Point out each Plasmodium parasite.
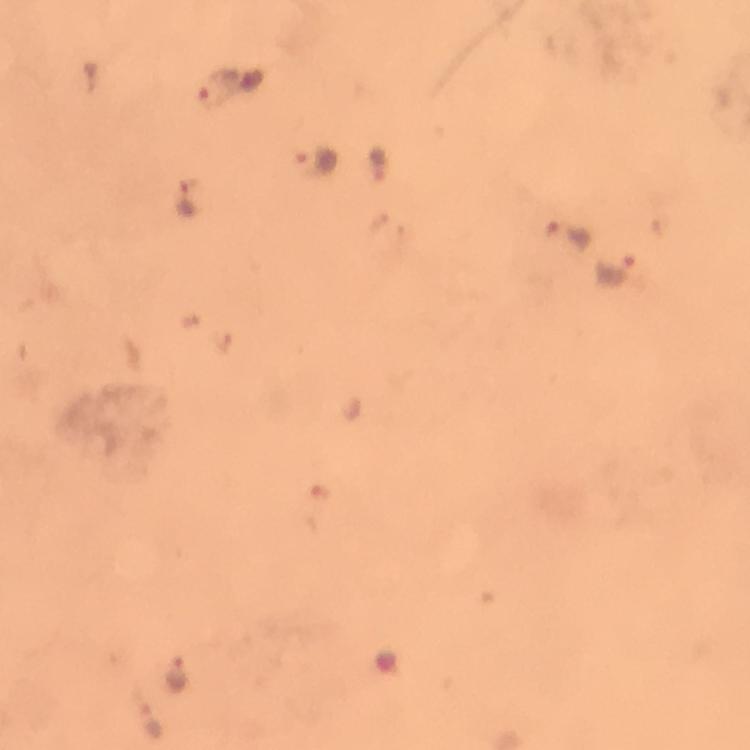

Approximate object centers, in pixels from the top-left corner.
Plasmodium parasites: (x=231, y=91), (x=318, y=163), (x=189, y=199), (x=568, y=236), (x=617, y=268), (x=178, y=673), (x=154, y=723).

Immersion oil applied. Photographed through the microscope with a smartphone camera. Thick blood smear. 100x magnification. Giemsa stain. Cropped region of a single field of view. Image is 750×750 pixels. From a diagnostic examination for malaria.